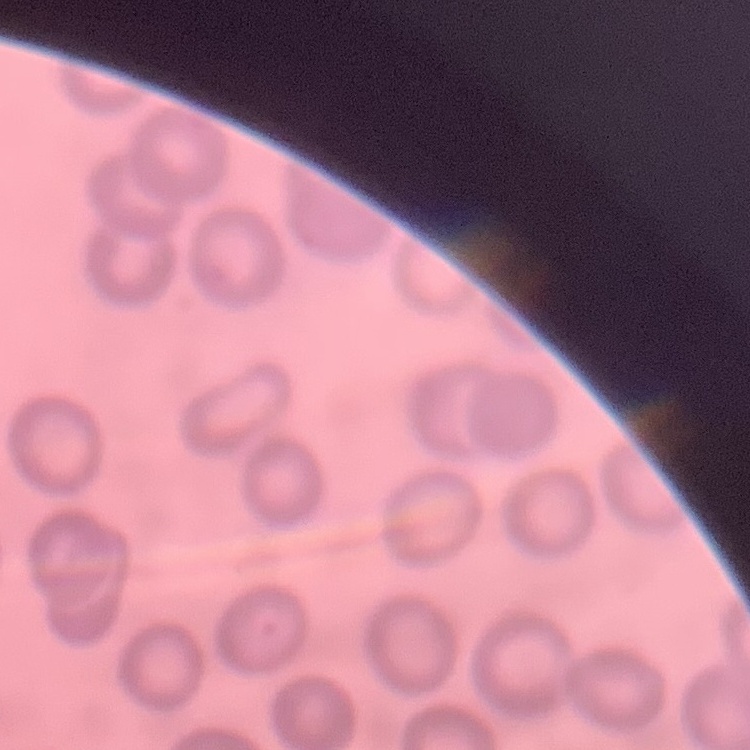 The erythrocytes show no rouleaux formation. Field's or Giemsa stain. Thin blood smear. Square crop of a larger photomicrograph.